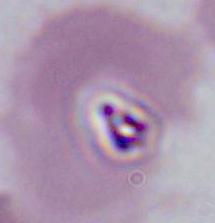

Captured at either 400x or 1000x magnification. A Plasmodium parasite is seen. Micrograph.